Locate every Plasmodium vivax-infected red blood cell.
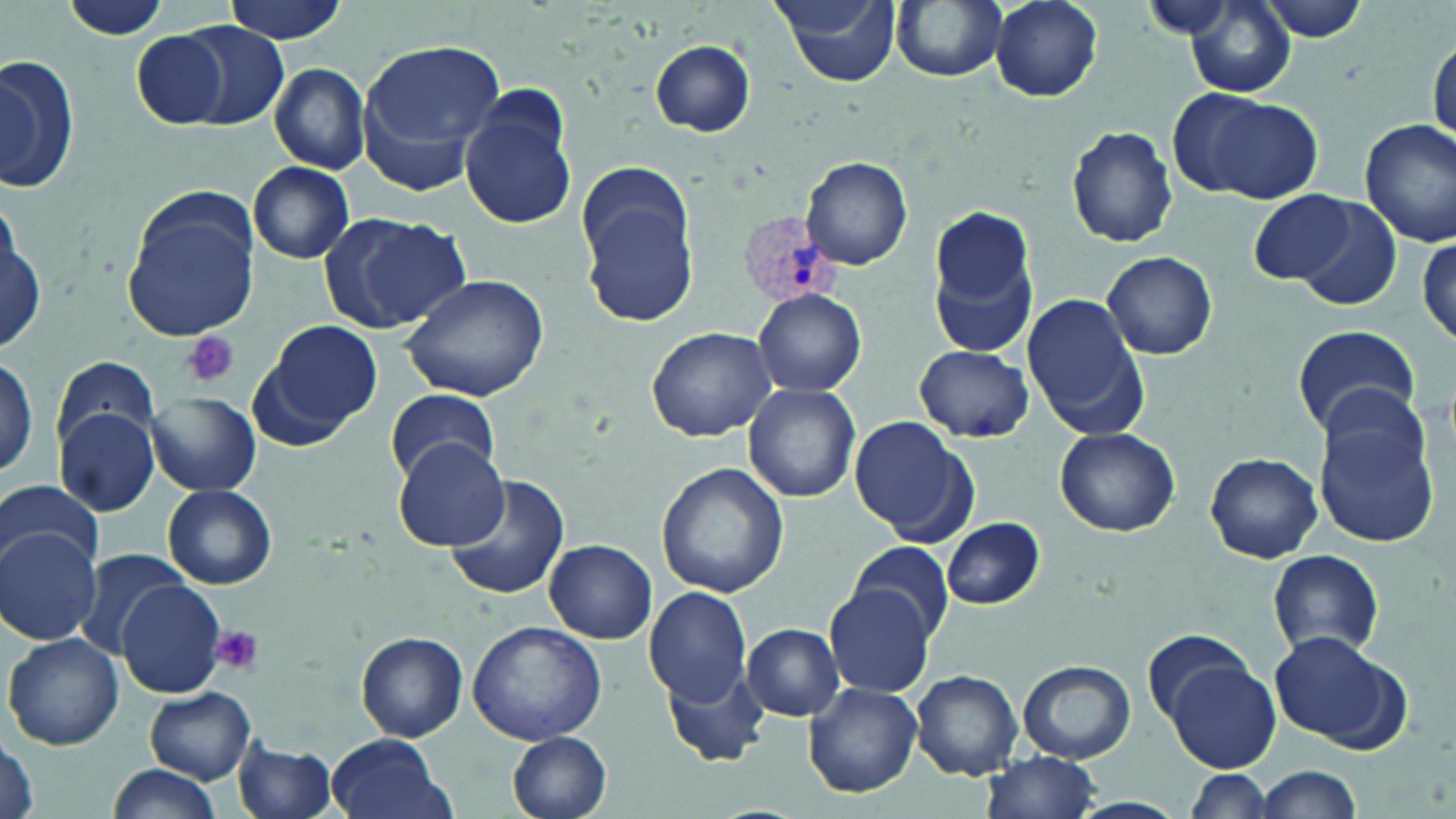

Approximate bounding boxes as (x1, y1, x2, y2) in pixels.
Plasmodium vivax-infected red blood cells: (740, 212, 842, 305).

Platelet locations: (181, 331, 240, 388), (208, 625, 265, 676). Uninfected red blood cell locations: (66, 0, 171, 43), (223, 0, 349, 43), (769, 0, 904, 88), (892, 0, 1009, 84), (990, 0, 1104, 102), (1181, 1, 1296, 98), (1251, 1, 1372, 43), (177, 23, 290, 129), (131, 30, 229, 129), (1429, 37, 1455, 149), (360, 38, 506, 174), (648, 39, 757, 137), (0, 54, 78, 197), (268, 63, 370, 175), (458, 89, 577, 231), (1180, 90, 1323, 202), (1358, 119, 1456, 247), (1066, 125, 1178, 248), (802, 157, 912, 271), (575, 161, 697, 327), (249, 162, 356, 264), (120, 188, 259, 342), (1247, 189, 1361, 286), (1293, 196, 1404, 312), (926, 203, 1041, 358), (317, 209, 469, 336), (2, 215, 45, 355), (1417, 232, 1454, 350), (1102, 250, 1217, 359), (400, 273, 553, 403), (752, 288, 867, 398), (1022, 293, 1149, 440), (250, 320, 383, 446), (1292, 324, 1422, 441), (645, 325, 778, 441), (915, 344, 1033, 443), (0, 350, 42, 483), (50, 354, 160, 452), (743, 383, 861, 503), (384, 387, 499, 485), (145, 393, 261, 495), (1314, 405, 1440, 547), (54, 407, 160, 516), (849, 418, 974, 542), (1055, 428, 1180, 536), (391, 438, 508, 550), (1205, 451, 1323, 564), (657, 462, 788, 598), (444, 472, 572, 602), (0, 478, 100, 572), (162, 485, 277, 590), (940, 516, 1045, 609), (0, 527, 102, 644), (545, 540, 657, 643), (850, 542, 953, 643), (72, 547, 195, 658), (1266, 550, 1385, 658), (117, 578, 227, 698), (826, 581, 935, 696), (643, 588, 752, 710), (466, 620, 608, 747), (742, 623, 846, 722), (1143, 628, 1258, 726), (1266, 630, 1406, 747), (358, 632, 467, 741), (3, 633, 123, 751), (1166, 657, 1280, 772), (658, 659, 767, 766), (1018, 661, 1135, 763), (912, 670, 1024, 779), (804, 683, 921, 797), (145, 688, 256, 784), (508, 731, 612, 819), (0, 733, 39, 819), (326, 733, 455, 819), (233, 735, 341, 819), (978, 752, 1106, 819), (103, 764, 225, 819), (1249, 765, 1364, 819), (1182, 768, 1277, 818). Slide-level diagnosis: Plasmodium vivax. Captured at 1000x magnification. May-Grünwald-Giemsa stain. Single field of view. Optical microscopy. Thin blood film. Image is 1456×819 pixels.